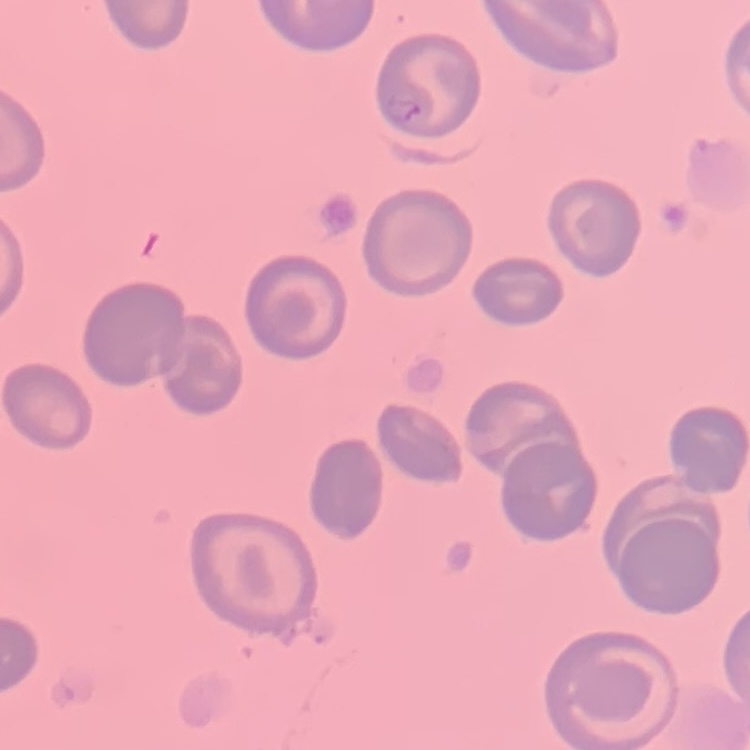

Summary:
  - Erythrocyte morphology: no rouleaux formation
  - Stain: Field's or Giemsa
  - Preparation: thin blood film
  - Image type: one tile cut from a larger photomicrograph